Locate every blood parasite and identify its species.
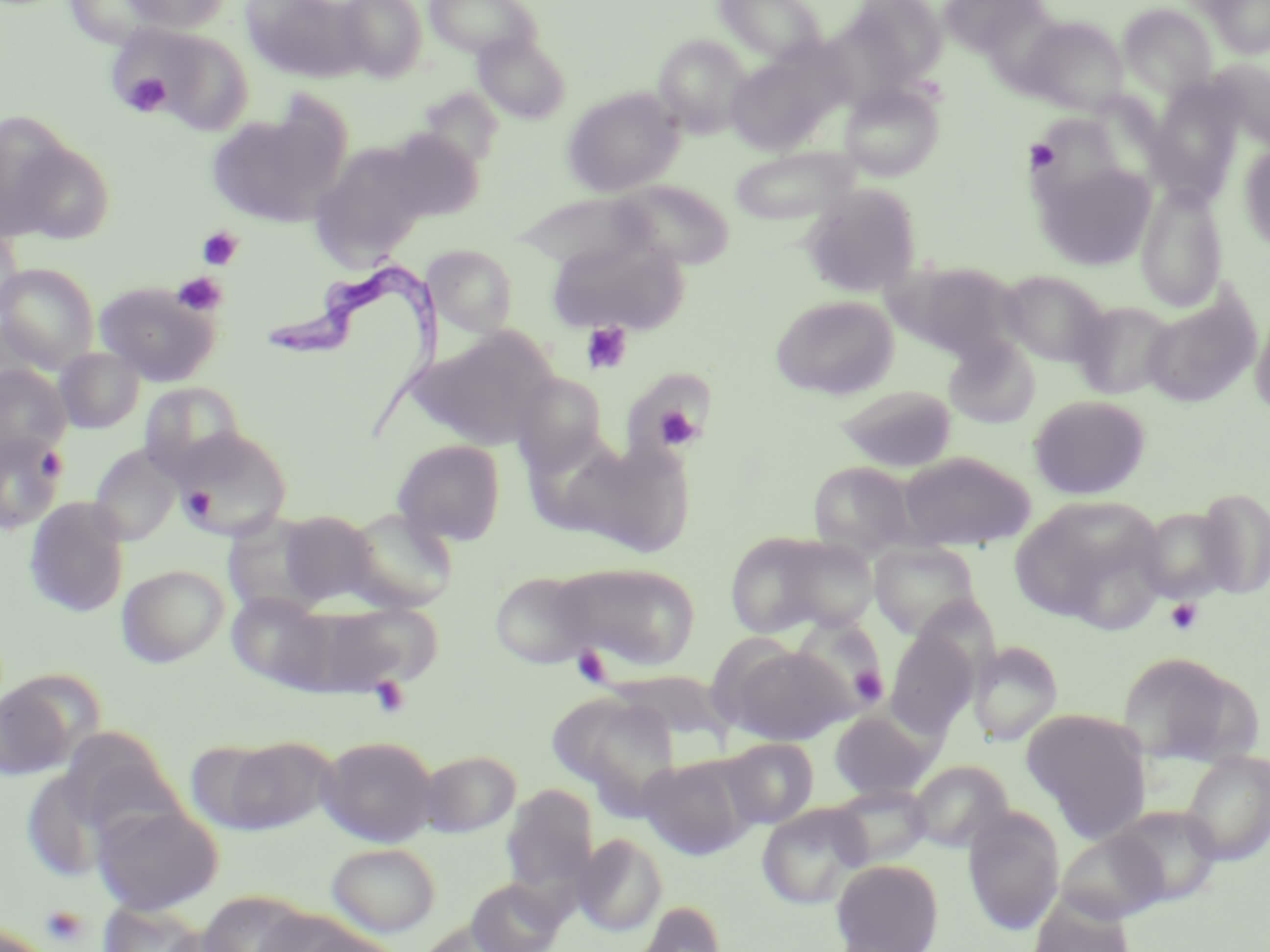
Approximate bounding boxes as (x1,y1)-(x2,y2) corner pairs in pixels.
Trypanosoma brucei: (274,269)-(449,439).
No Plasmodium falciparum, Plasmodium ovale, Plasmodium malariae, Plasmodium vivax, or Babesia divergens observed.

Summary:
  - Uninfected red blood cell locations: (63,0)-(171,50), (121,0)-(234,33), (241,0)-(366,82), (335,0)-(428,81), (423,0)-(541,62), (714,0)-(829,65), (841,0)-(948,90), (1204,1)-(1270,58), (1117,2)-(1218,101), (1018,15)-(1128,116), (133,27)-(256,135), (472,33)-(572,124), (653,33)-(752,138), (724,55)-(831,154), (1210,58)-(1269,145), (839,82)-(944,181), (1145,84)-(1244,204), (563,87)-(684,196), (205,105)-(349,228), (1029,113)-(1129,201), (1,119)-(96,244), (382,127)-(484,222), (309,142)-(430,267), (1238,143)-(1270,253), (729,145)-(861,227), (1036,163)-(1155,271), (610,180)-(735,270), (1136,183)-(1228,313), (800,184)-(921,298), (507,192)-(657,269), (0,225)-(24,325), (547,236)-(689,335), (425,246)-(519,338), (898,261)-(1025,362), (0,262)-(99,369), (998,269)-(1111,367), (94,282)-(220,386), (1141,288)-(1260,408), (770,295)-(899,400), (1071,301)-(1178,400), (1251,309)-(1270,420), (412,327)-(558,450), (944,337)-(1041,429), (55,347)-(145,433), (0,364)-(71,459), (513,373)-(609,474), (139,382)-(246,480), (835,384)-(957,473), (1029,395)-(1150,499), (171,427)-(293,541), (0,431)-(67,535), (561,439)-(694,557), (393,440)-(506,545), (89,445)-(182,545), (899,450)-(1035,550), (807,462)-(918,559), (1193,487)-(1270,598), (1011,495)-(1166,629), (24,497)-(130,617), (1133,505)-(1239,604), (343,508)-(459,613), (278,511)-(381,606), (723,531)-(845,638), (868,541)-(983,641), (549,562)-(701,672), (117,564)-(229,667), (490,569)-(601,669), (227,592)-(335,689), (296,600)-(444,694), (788,616)-(887,717), (885,626)-(980,738), (968,640)-(1064,745), (717,643)-(852,745), (1116,651)-(1256,766), (0,679)-(79,782), (548,691)-(682,810), (1022,708)-(1152,835), (828,709)-(938,801), (57,729)-(186,840), (215,735)-(336,833), (318,735)-(438,847), (721,738)-(818,829), (1180,749)-(1270,866), (420,750)-(520,836), (638,756)-(754,859), (909,759)-(1013,852), (501,784)-(599,901), (831,786)-(931,868), (92,802)-(223,914), (757,803)-(872,908), (1110,804)-(1224,906), (963,808)-(1065,934), (1055,830)-(1169,923), (573,833)-(668,936), (327,842)-(441,937), (832,859)-(943,951), (466,878)-(567,952), (196,890)-(315,952), (1029,895)-(1135,952), (627,900)-(727,952), (97,902)-(205,952), (253,908)-(362,952), (292,923)-(406,952)
  - Platelet locations: (123,72)-(173,117), (1025,139)-(1060,173), (198,227)-(243,270), (172,272)-(227,316), (581,322)-(632,375), (652,403)-(702,450), (181,487)-(216,522), (1165,598)-(1204,636), (572,648)-(612,685), (851,666)-(888,706), (368,676)-(412,719), (40,905)-(89,947)
  - Slide-level diagnosis: Trypanosoma brucei
  - Field of view: one of a larger specimen
  - Image size: 1270×952 pixels
  - Preparation: thin blood smear
  - Stain: May-Grünwald-Giemsa
  - Modality: optical microscopy
  - Magnification: 1000x